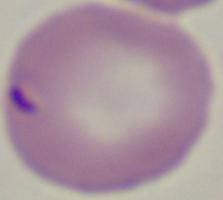
1000x magnification. A Babesia parasite is shown. Micrograph.